Give the position of every malaria parasite.
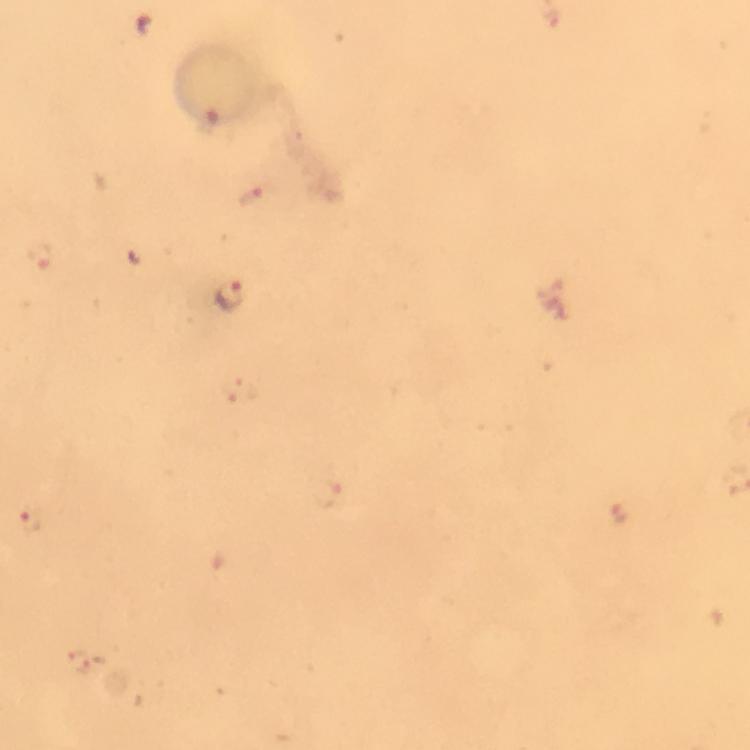
Approximate centers as {x, y} in pixels.
Malaria parasites: {255, 195}, {42, 258}, {230, 296}, {619, 515}, {30, 521}.

Summary:
  - Stain: Giemsa
  - Preparation: thick smear
  - Capture: smartphone photograph through a microscope
  - Context: from a diagnostic examination for malaria
  - Cropped from: a single field of view
  - Magnification: 100x
  - Immersion oil: applied
  - Image size: 750×750 pixels